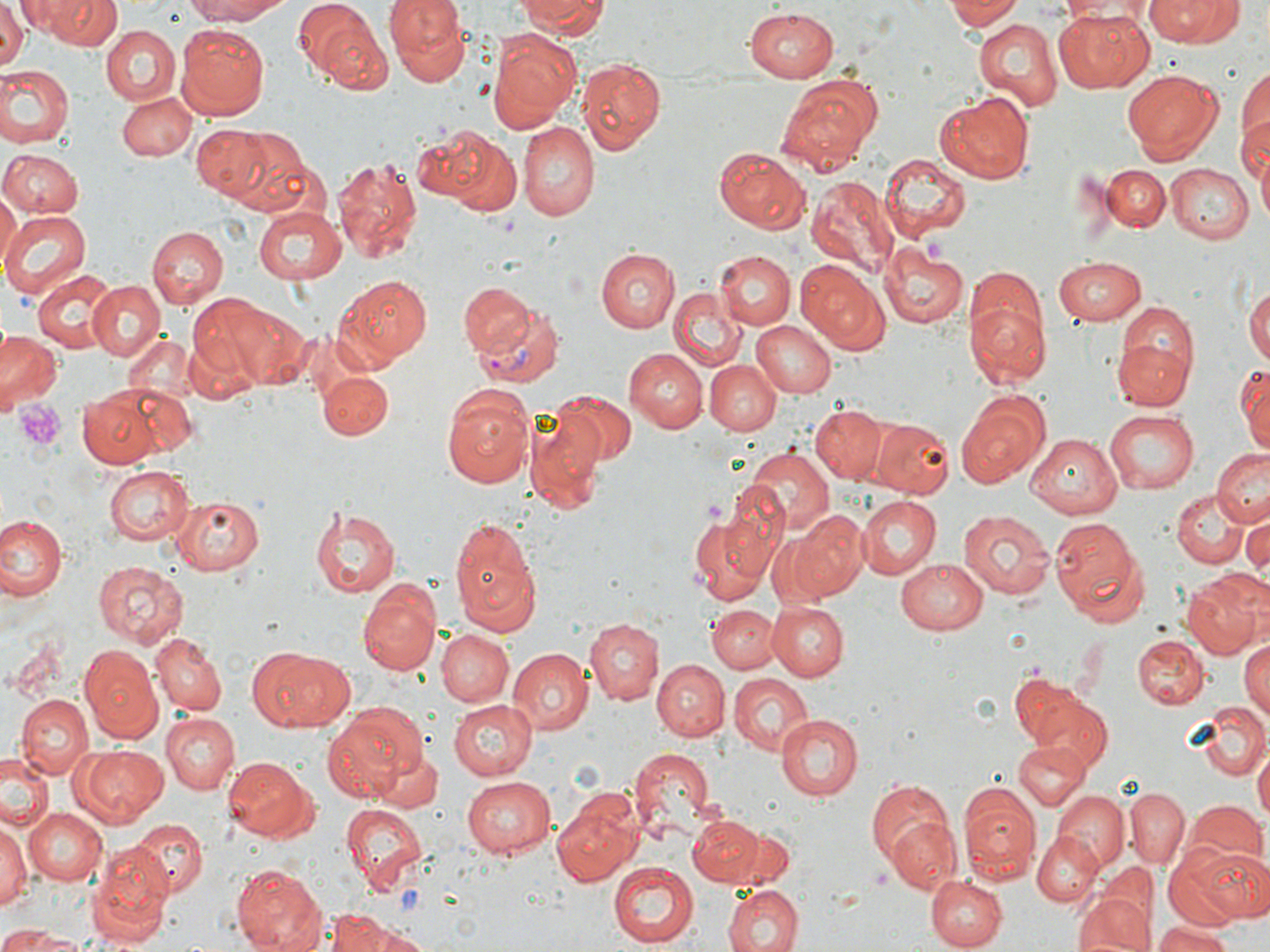
slide-level diagnosis = Plasmodium vivax
preparation = thin blood smear
stain = May-Grünwald-Giemsa
uninfected red blood cell locations = approximate bounding boxes as [x1, y1, x2, y2] in pixels: [47, 0, 119, 51], [183, 0, 293, 24], [385, 0, 468, 83], [519, 0, 608, 37], [944, 0, 1020, 32], [1147, 0, 1243, 44], [0, 1, 25, 73], [19, 1, 100, 40], [295, 1, 383, 82], [1055, 6, 1154, 91], [743, 8, 839, 83], [972, 18, 1064, 110], [321, 19, 392, 97], [176, 24, 273, 119], [102, 26, 179, 104], [489, 29, 579, 131], [578, 55, 668, 157], [1235, 58, 1270, 170], [0, 65, 73, 147], [1120, 69, 1224, 165], [781, 77, 881, 167], [116, 91, 196, 160], [934, 92, 1034, 184], [518, 122, 598, 221], [191, 125, 272, 200], [217, 126, 312, 213], [428, 128, 520, 214], [1254, 140, 1270, 235], [714, 149, 814, 233], [0, 150, 82, 216], [879, 154, 970, 242], [331, 156, 423, 264], [1165, 163, 1253, 243], [1102, 164, 1169, 231], [807, 175, 898, 274], [0, 193, 18, 273], [255, 204, 351, 284], [1, 209, 91, 297], [148, 225, 225, 308], [879, 245, 969, 330], [597, 249, 679, 332], [715, 251, 794, 329], [713, 256, 880, 336], [1055, 256, 1147, 324], [797, 263, 888, 354], [31, 269, 123, 353], [334, 274, 433, 365], [962, 275, 1052, 390], [89, 278, 165, 362], [460, 284, 535, 354], [1246, 285, 1270, 374], [668, 288, 745, 371], [191, 293, 305, 394], [750, 319, 835, 397], [1112, 319, 1196, 414], [0, 328, 61, 414], [121, 332, 198, 404], [625, 346, 709, 432], [1236, 358, 1269, 458], [705, 360, 779, 438], [106, 365, 199, 461], [317, 370, 394, 440], [441, 389, 533, 489], [77, 391, 165, 466], [554, 393, 636, 468], [956, 394, 1048, 487], [810, 405, 885, 483], [1103, 409, 1198, 494], [526, 414, 606, 512], [872, 417, 956, 499], [1027, 420, 1199, 506], [1026, 431, 1120, 515], [744, 447, 832, 534], [1213, 448, 1270, 527], [103, 465, 194, 546], [1172, 490, 1247, 567], [169, 496, 266, 575], [856, 496, 941, 579], [310, 504, 401, 598], [958, 509, 1055, 601], [686, 510, 776, 607], [788, 511, 868, 599], [1241, 512, 1270, 579], [1, 514, 67, 604], [450, 519, 541, 637], [1050, 520, 1149, 627], [897, 558, 989, 635], [93, 560, 188, 648], [1183, 568, 1269, 658], [357, 575, 442, 677], [768, 601, 847, 679], [708, 603, 777, 673], [585, 618, 662, 705], [436, 627, 513, 707], [152, 632, 229, 715], [1133, 633, 1207, 709], [1238, 639, 1270, 719], [252, 645, 354, 731], [79, 646, 163, 742], [505, 647, 590, 734], [652, 659, 729, 740], [726, 672, 815, 757], [1008, 673, 1097, 757], [15, 694, 93, 780], [1029, 694, 1115, 773], [446, 696, 535, 780], [1197, 700, 1268, 781], [322, 701, 423, 803], [162, 712, 238, 794], [774, 713, 863, 803], [1015, 737, 1089, 809], [77, 745, 168, 824], [372, 746, 443, 812], [626, 746, 715, 835], [1252, 746, 1269, 821], [0, 753, 53, 832], [222, 755, 320, 844], [462, 774, 560, 856], [866, 776, 960, 879], [958, 784, 1040, 883], [1125, 788, 1188, 867], [1052, 791, 1127, 868], [550, 793, 644, 885], [1188, 799, 1266, 866], [338, 801, 429, 893], [26, 805, 109, 886], [687, 814, 765, 884], [885, 815, 961, 894], [133, 820, 207, 896], [0, 823, 30, 912], [732, 829, 796, 886], [1032, 830, 1105, 907], [1170, 843, 1269, 926], [86, 845, 173, 946], [609, 863, 700, 947], [1095, 863, 1157, 931], [229, 864, 325, 952], [925, 875, 1004, 949], [720, 882, 805, 952], [1078, 885, 1155, 952], [323, 911, 409, 952], [1156, 920, 1234, 952], [2, 924, 87, 950]
platelet locations = approximate bounding boxes as [x1, y1, x2, y2] in pixels: [927, 240, 945, 267], [17, 399, 64, 453]
Plasmodium vivax-infected red blood cell locations = approximate bounding boxes as [x1, y1, x2, y2] in pixels: [469, 299, 565, 393]
magnification = 1000x
modality = optical microscopy
image size = 1270×952 pixels
field of view = single